Identify the preparation type.
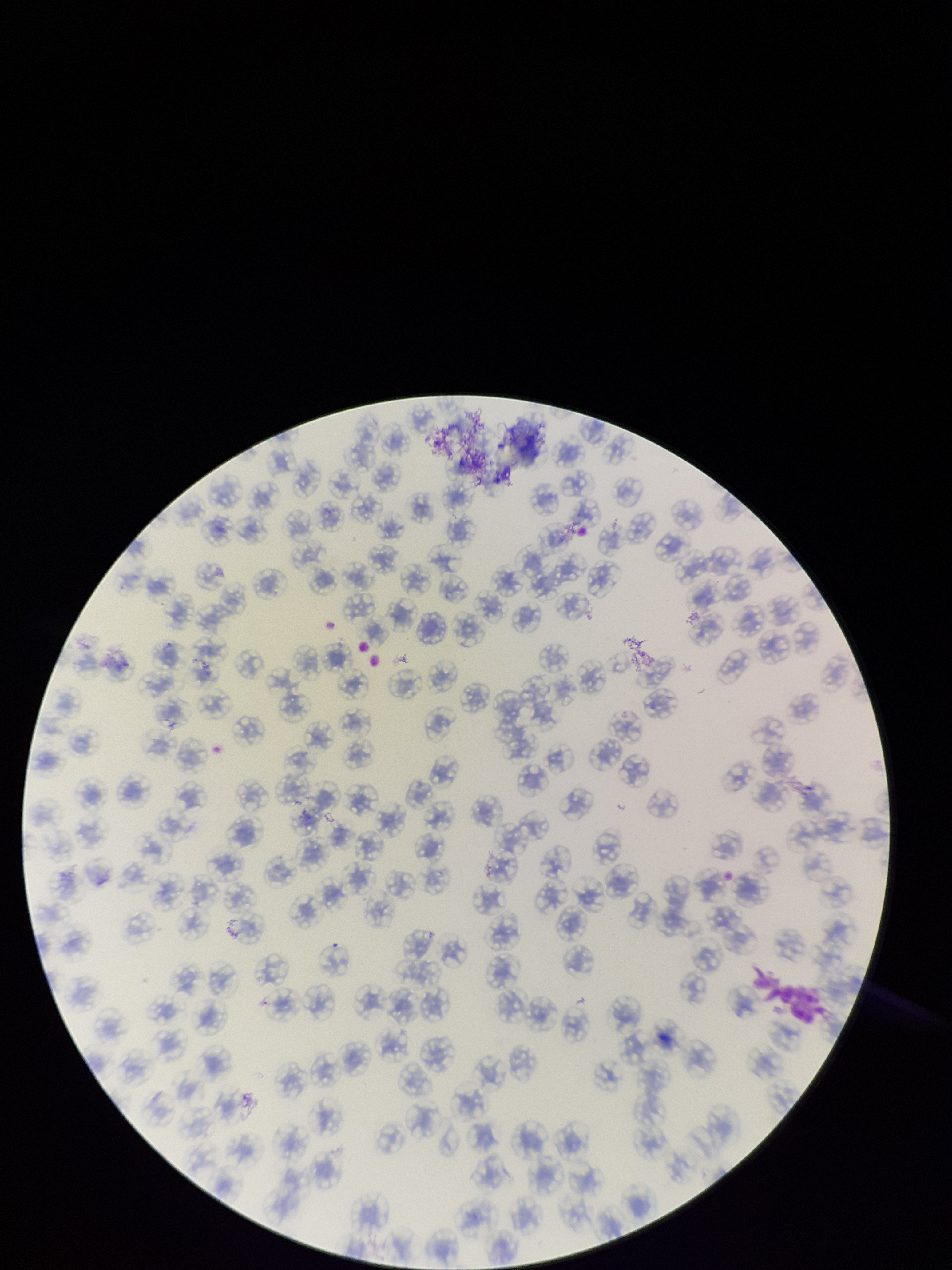
Thin.

Giemsa stain. One field from this slide. Parasitized red blood cells: none identified. Parasitized red blood cell count: 0. Patient malaria status: negative. Image is 952×1270 pixels. Smartphone photograph taken through the eyepiece of a microscope. Red blood cell count: 133.